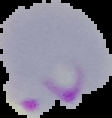 Segmented cell region on a black background. Result: Plasmodium parasites detected. Image is 112×118 pixels. From a thin blood smear.